Describe the morphology of the red blood cells.
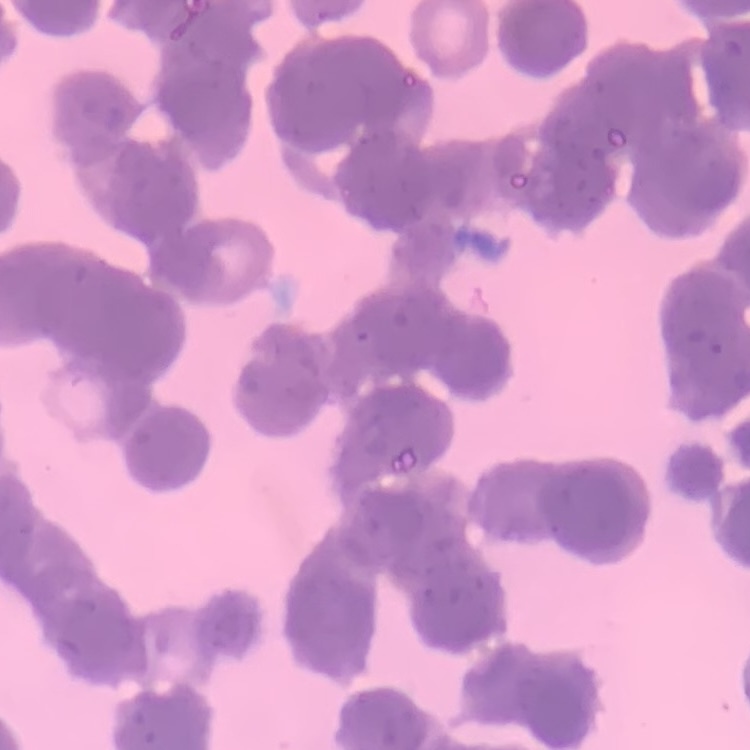
They show rouleaux formation.

Summary:
  - Image type: one tile cut from a larger photomicrograph
  - Preparation: thin blood film
  - Stain: Field's or Giemsa